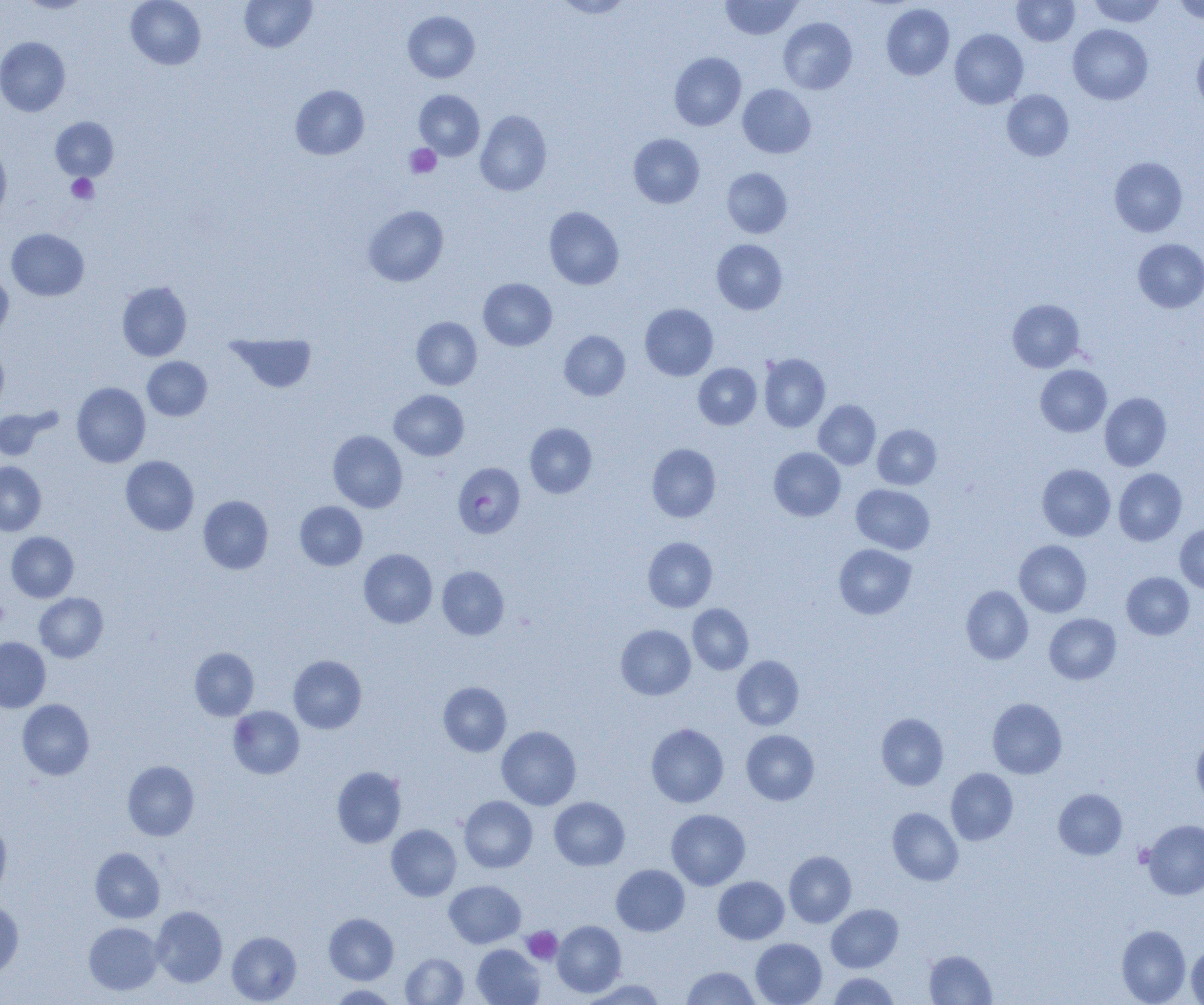 Approximate bounding boxes as (x1,y1)-(x2,y2) corner pairs in pixels. Uninfected red blood cell locations: (19,0)-(92,13), (125,0)-(206,69), (239,0)-(317,52), (554,0)-(633,18), (1012,0)-(1079,46), (1088,0)-(1166,27), (1174,0)-(1204,24), (721,1)-(801,39), (881,4)-(954,80), (403,11)-(479,82), (779,18)-(857,94), (1068,24)-(1153,104), (950,29)-(1028,109), (0,37)-(70,116), (1192,39)-(1204,113), (669,52)-(746,131), (737,84)-(816,158), (290,85)-(369,160), (414,90)-(484,160), (1002,90)-(1074,161), (475,110)-(552,195), (50,117)-(118,181), (628,134)-(704,208), (0,142)-(11,221), (1109,157)-(1187,237), (722,168)-(792,238), (363,205)-(448,286), (544,206)-(624,290), (7,228)-(89,301), (712,239)-(787,314), (1133,239)-(1204,313), (0,269)-(13,339), (478,278)-(557,351), (117,281)-(192,361), (1008,299)-(1084,372), (640,304)-(718,381), (411,316)-(482,390), (559,331)-(630,400), (227,334)-(316,393), (0,341)-(8,415), (759,353)-(830,432), (142,357)-(212,420), (693,363)-(761,429), (1036,365)-(1111,436), (71,382)-(150,467), (389,390)-(469,460), (1100,392)-(1172,471), (813,400)-(880,470), (0,407)-(57,461), (525,423)-(597,498), (872,424)-(941,489), (328,430)-(407,512), (646,443)-(721,522), (769,448)-(845,521), (120,455)-(199,535), (0,462)-(46,535), (1037,464)-(1115,541), (1114,468)-(1186,546), (852,484)-(935,554), (198,496)-(273,574), (295,501)-(367,570), (1175,524)-(1204,593), (6,531)-(79,602), (643,537)-(717,612), (1014,540)-(1092,617), (834,544)-(916,619), (359,549)-(437,628), (437,566)-(509,640), (1122,572)-(1194,639), (961,586)-(1033,664), (34,593)-(108,662), (687,604)-(753,674), (1044,613)-(1121,684), (616,625)-(695,700), (0,637)-(50,712), (190,647)-(259,720), (288,655)-(366,734), (732,655)-(804,730), (438,682)-(511,756), (987,698)-(1066,778), (17,699)-(94,780), (228,706)-(304,779), (876,713)-(948,790), (646,723)-(728,807), (497,726)-(581,810), (741,730)-(819,805), (1192,734)-(1204,810), (122,760)-(199,840), (332,766)-(406,848), (945,768)-(1018,845), (1053,788)-(1127,859), (459,796)-(537,872), (549,797)-(629,870), (887,808)-(963,885), (666,809)-(750,889), (1142,819)-(1204,900), (0,820)-(10,897), (386,824)-(461,901), (90,847)-(164,923), (784,851)-(856,927), (611,864)-(689,936), (712,876)-(789,944), (444,880)-(525,948), (0,900)-(23,977), (826,904)-(903,972), (151,906)-(227,987), (324,913)-(399,984), (552,920)-(626,997), (84,922)-(163,995), (1116,925)-(1191,1005), (227,931)-(301,1004), (751,938)-(827,1005), (472,944)-(545,1005), (1187,945)-(1204,1004), (924,950)-(996,1004), (401,953)-(468,1004), (682,966)-(760,1004), (828,972)-(899,1004), (582,979)-(666,1005), (329,985)-(399,1004). Plasmodium falciparum-infected red blood cell locations: (453,462)-(525,538). Platelet locations: (405,144)-(441,179), (66,174)-(98,204), (0,598)-(8,630), (522,927)-(562,964). Slide-level diagnosis: Plasmodium falciparum. Light microscopy. Captured at 1000x magnification. One field of a larger specimen. Image is 1204×1005 pixels. Thin blood smear.